Comment on the morphology of the red blood cells.
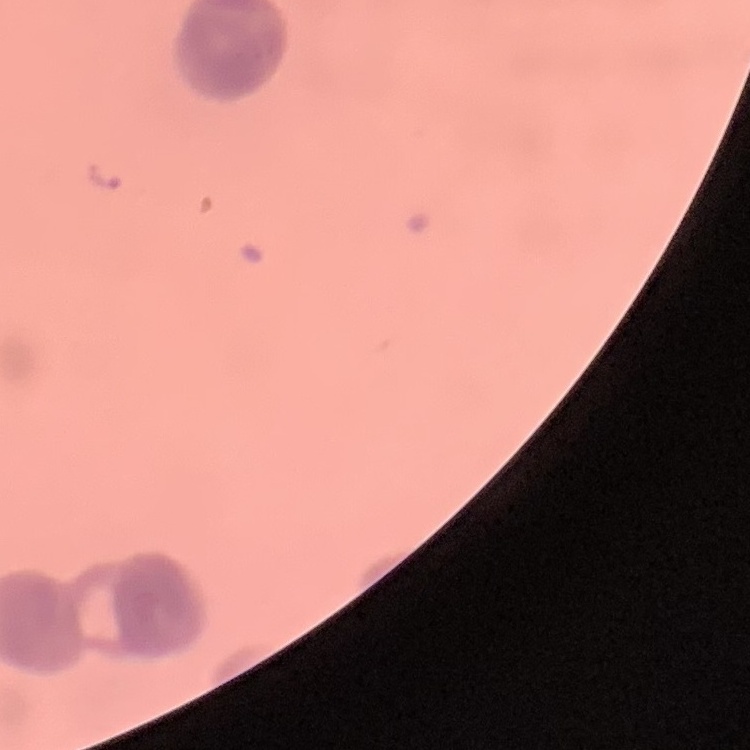

Rouleaux formation.

Thin peripheral smear. Stained with either Field's or Giemsa. Square crop of a larger photomicrograph.